Locate every Plasmodium falciparum-infected red blood cell.
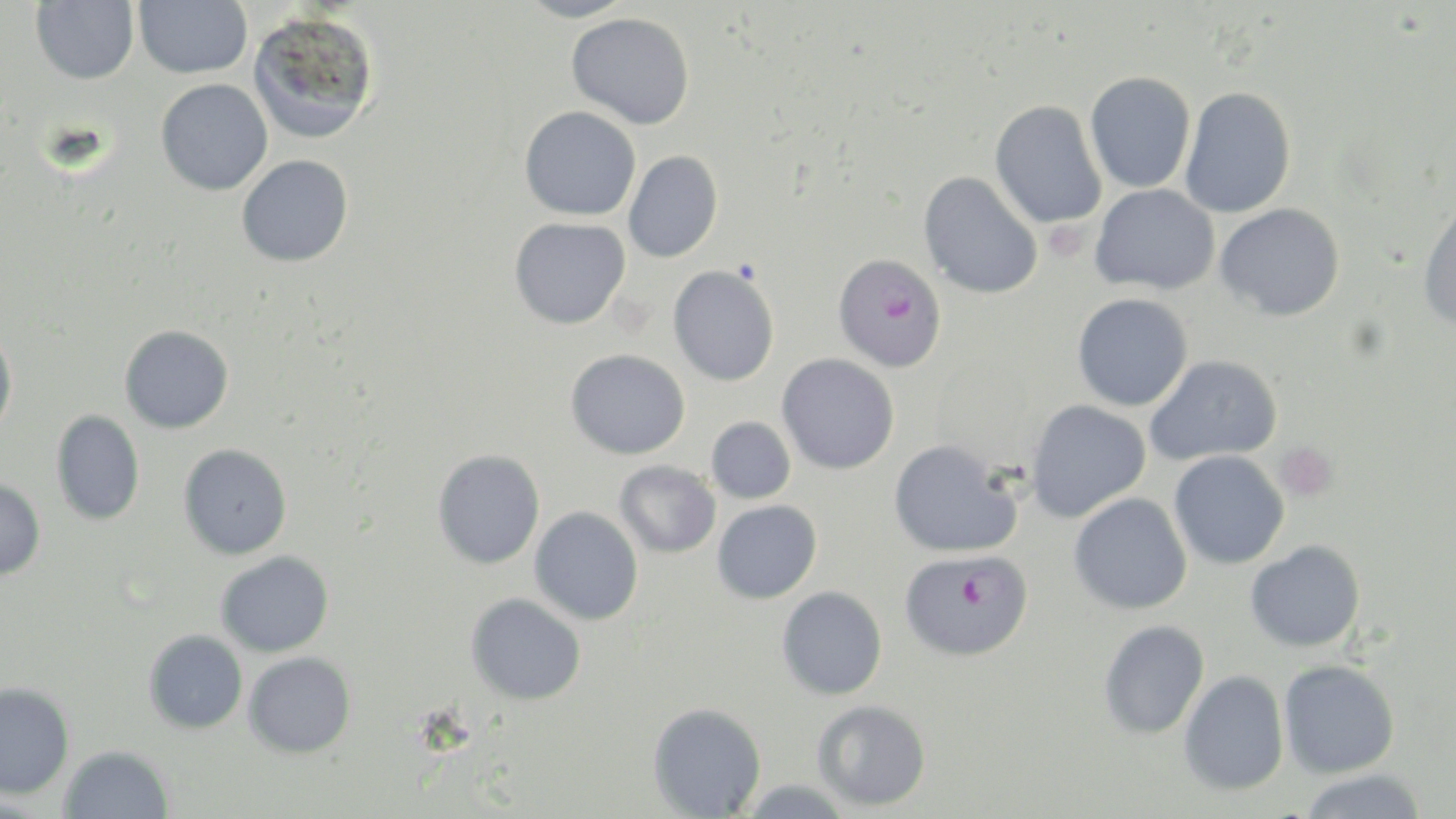
Approximate bounding boxes as (x1,y1)-(x2,y2) corner pairs in pixels.
Plasmodium falciparum-infected red blood cells: (833,253)-(947,373), (900,549)-(1033,660).

slide_level_diagnosis: Plasmodium falciparum
stain: May-Grünwald-Giemsa
field_of_view: single
preparation: thin blood film
magnification: 1000x
image_size: 1456×819 pixels
uninfected_red_blood_cell_locations: 'approximate bounding boxes as (x1,y1)-(x2,y2) corner pairs in pixels: (31,0)-(139,84), (134,0)-(252,78), (515,0)-(638,23), (248,10)-(380,144), (565,13)-(695,129), (1084,71)-(1196,193), (156,79)-(272,196), (1179,85)-(1296,218), (990,100)-(1107,228), (519,106)-(641,221), (623,150)-(723,263), (236,154)-(354,267), (918,171)-(1043,299), (1090,183)-(1220,295), (1417,197)-(1456,331), (1215,203)-(1345,321), (509,217)-(631,330), (668,265)-(780,386), (1072,293)-(1193,411), (120,325)-(234,434), (0,328)-(17,438), (565,348)-(690,459), (777,353)-(900,475), (1145,354)-(1283,466), (1026,399)-(1151,522), (52,410)-(145,525), (706,417)-(796,503), (888,439)-(1022,558), (179,444)-(292,559), (432,449)-(545,569), (1168,450)-(1289,569), (615,460)-(721,558), (0,479)-(45,580), (1068,493)-(1193,615), (712,500)-(822,604), (529,506)-(644,625), (1245,540)-(1366,652), (216,551)-(334,657), (776,586)-(888,700), (466,592)-(586,705), (1098,620)-(1210,740), (144,629)-(248,734), (244,652)-(356,758), (1278,659)-(1400,778), (1178,669)-(1290,795), (0,682)-(75,800), (811,699)-(931,811), (647,702)-(766,818), (59,745)-(173,819), (1297,769)-(1427,819)'
platelet_locations: 'approximate bounding boxes as (x1,y1)-(x2,y2) corner pairs in pixels: (1047,226)-(1079,261), (1274,442)-(1339,502)'
modality: light microscopy